Report the malaria status of this cell.
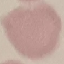

It is uninfected.

Photographed with a smartphone camera at the microscope eyepiece. Thin blood film. Giemsa-stained preparation. Automatically extracted cell patch, resized to 64 × 64 pixels.